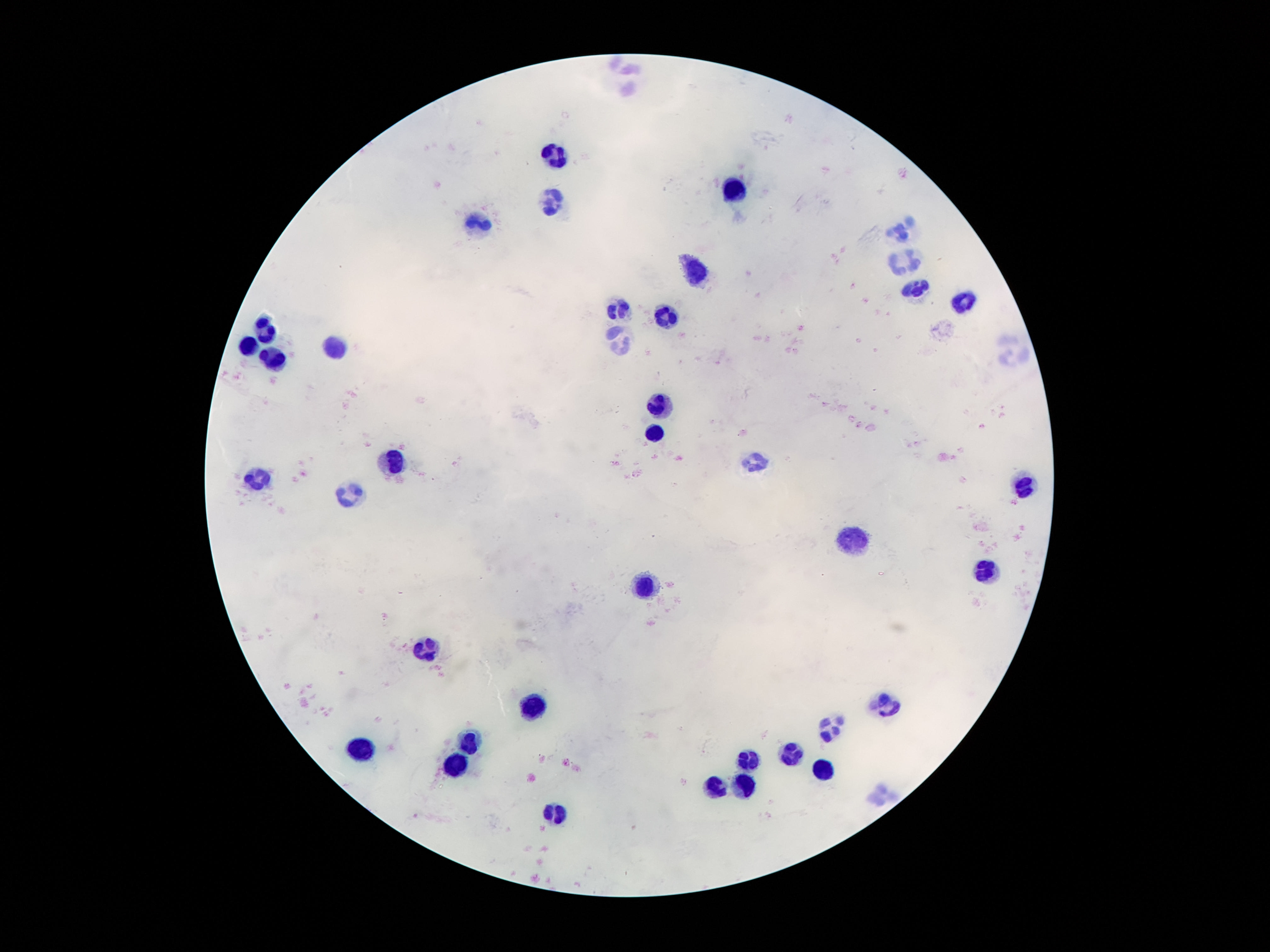

stain = Giemsa
capture = smartphone camera through the microscope eyepiece
magnification = 100x
patient malaria status = not infected
leukocyte locations = approximate centers as {x, y} in pixels: {622, 77}, {553, 152}, {735, 191}, {551, 203}, {474, 224}, {900, 227}, {900, 260}, {695, 270}, {916, 288}, {962, 302}, {618, 311}, {662, 317}, {266, 330}, {620, 342}, {248, 348}, {335, 348}, {1013, 355}, {275, 361}, {660, 406}, {653, 435}, {757, 457}, {390, 458}, {255, 482}, {1022, 488}, {350, 494}, {852, 543}, {982, 571}, {644, 585}, {427, 647}, {533, 706}, {885, 706}, {832, 728}, {469, 745}, {357, 752}, {788, 757}, {750, 761}, {456, 763}, {821, 770}, {741, 781}, {717, 785}, {878, 794}, {558, 815}
field of view = single
image size = 1270×952 pixels
preparation = thick blood smear